Identify the blood parasite species.
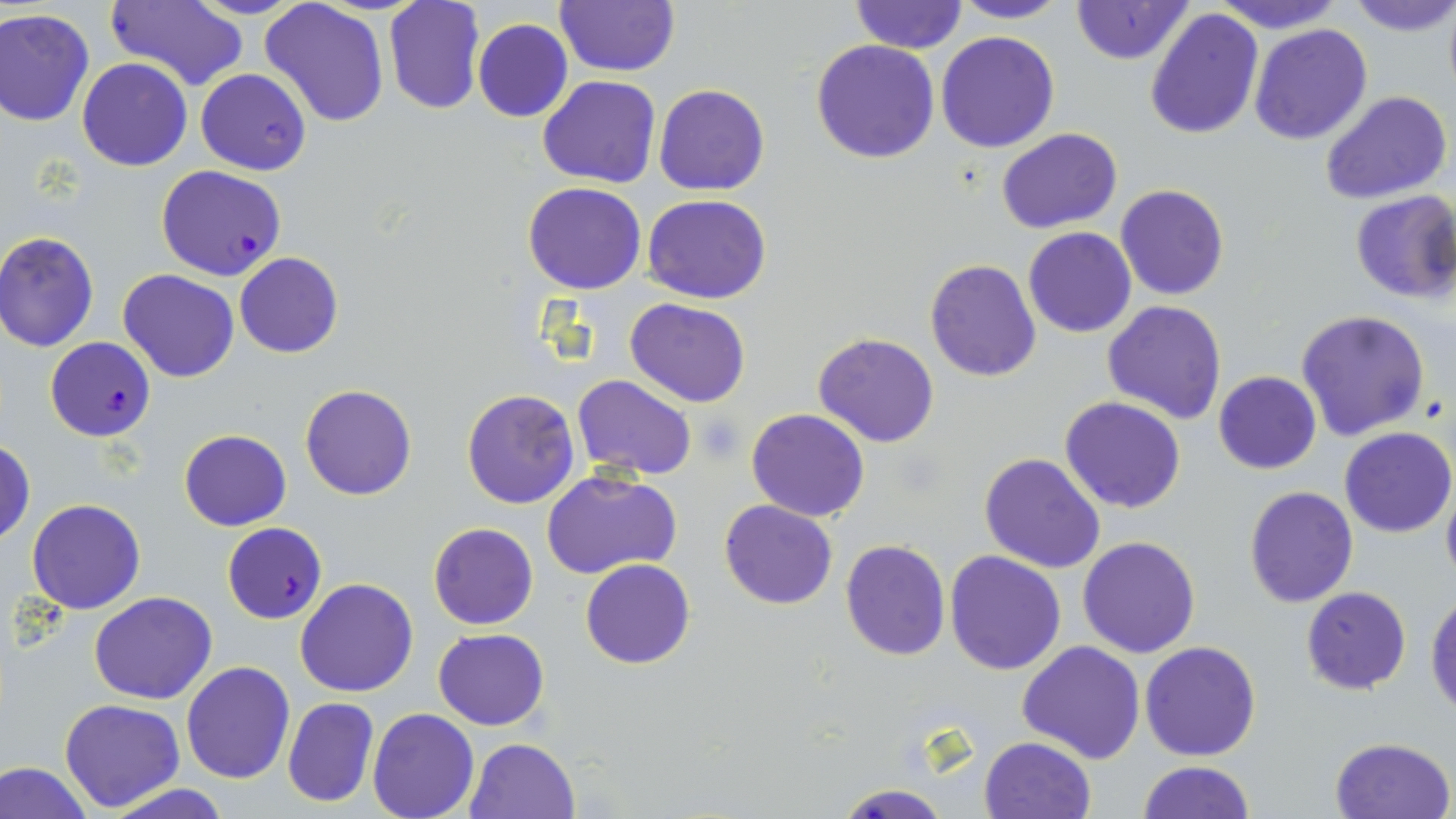
Plasmodium falciparum.

image size = 1456×819 pixels
Plasmodium falciparum-infected red blood cell locations = approximate bounding boxes as (x1,y1)-(x2,y2) corner pairs in pixels: (156,165)-(287,281), (45,338)-(157,441), (226,525)-(348,629)
stain = May-Grünwald-Giemsa
preparation = thin blood film
uninfected red blood cell locations = approximate bounding boxes as (x1,y1)-(x2,y2) corner pairs in pixels: (383,0)-(485,116), (554,0)-(678,76), (949,0)-(1070,24), (1071,0)-(1192,65), (1210,0)-(1346,33), (1346,0)-(1456,37), (100,1)-(250,92), (851,1)-(966,52), (260,2)-(391,128), (1146,7)-(1264,141), (0,8)-(96,126), (473,18)-(574,121), (1249,24)-(1374,146), (936,30)-(1059,152), (811,39)-(940,164), (77,58)-(192,171), (196,68)-(312,175), (537,75)-(661,188), (653,84)-(769,196), (1320,88)-(1453,205), (996,128)-(1123,235), (522,182)-(647,295), (1115,184)-(1230,300), (1349,190)-(1456,304), (642,195)-(771,305), (1023,226)-(1136,338), (1,231)-(99,352), (235,251)-(344,358), (924,259)-(1041,382), (119,269)-(238,383), (624,298)-(751,406), (1102,300)-(1228,423), (1296,309)-(1430,440), (591,312)-(744,473), (813,332)-(940,448), (1212,372)-(1323,475), (573,374)-(698,481), (300,384)-(416,500), (461,388)-(581,510), (1061,397)-(1185,513), (746,408)-(870,522), (1338,427)-(1454,538), (179,430)-(291,531), (1,440)-(35,545), (979,452)-(1107,574), (542,468)-(682,579), (1441,476)-(1456,594), (1243,485)-(1358,607), (26,498)-(146,614), (718,499)-(838,609), (428,523)-(538,630), (1078,536)-(1201,658), (840,537)-(951,660), (943,552)-(1066,675), (580,558)-(695,670), (295,578)-(419,697), (1299,586)-(1412,695), (89,591)-(218,705), (1426,593)-(1456,714), (432,628)-(549,731), (1016,640)-(1146,765), (1141,640)-(1261,762), (181,662)-(296,784), (282,697)-(379,807), (59,698)-(184,811), (367,709)-(480,819), (979,735)-(1096,819), (464,737)-(581,819), (1329,737)-(1456,819), (0,760)-(94,819), (1138,761)-(1254,817), (832,782)-(952,819), (98,783)-(238,818)
magnification = 1000x
field of view = one of a larger specimen
modality = light microscopy
platelet locations = approximate bounding boxes as (x1,y1)-(x2,y2) corner pairs in pixels: (694,415)-(746,462)